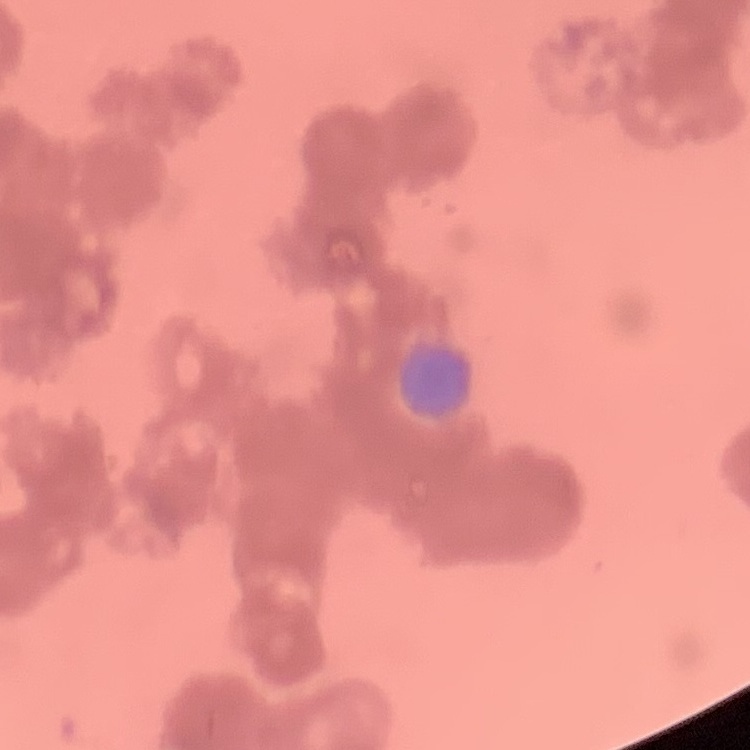
red blood cell morphology = rouleaux formation
stain = Field's or Giemsa
image type = square crop of a larger photomicrograph
preparation = thin blood smear